Assess this cell for malaria.
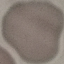

It is uninfected.

Summary:
  - Stain: Giemsa
  - Preparation: thin blood film
  - Capture: smartphone camera at the microscope eyepiece
  - Image type: cell patch, automatically extracted from a larger field of view and resized to 64 × 64 pixels